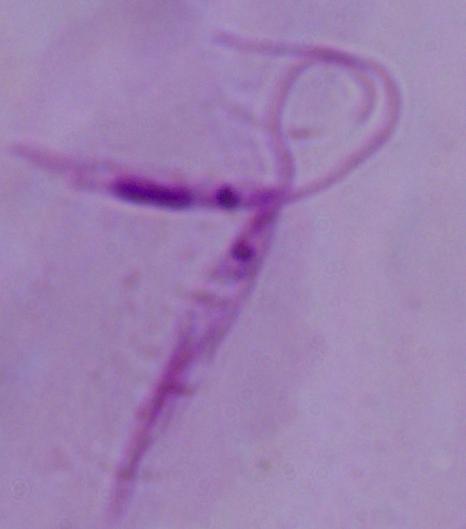
A Leishmania parasite is seen. Captured at 1000x magnification. Photomicrograph.